State which parasite is depicted.
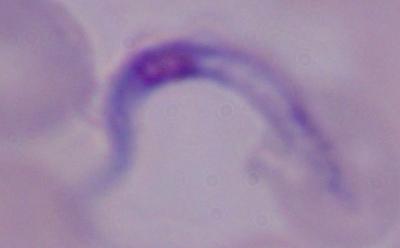

A trypanosome.

{
  "magnification": "1000x",
  "modality": "photomicrograph"
}